Report the malaria status of this cell.
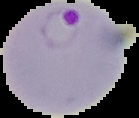

Parasitized.

image_type: cell region segmented out of the field of view; surrounding area masked to black
image_size: 139×118 pixels
preparation: thin blood smear